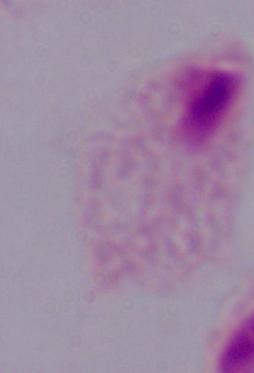

{
  "identification": "trichomonad",
  "modality": "photomicrograph",
  "magnification": "1000x"
}